Identify the preparation type.
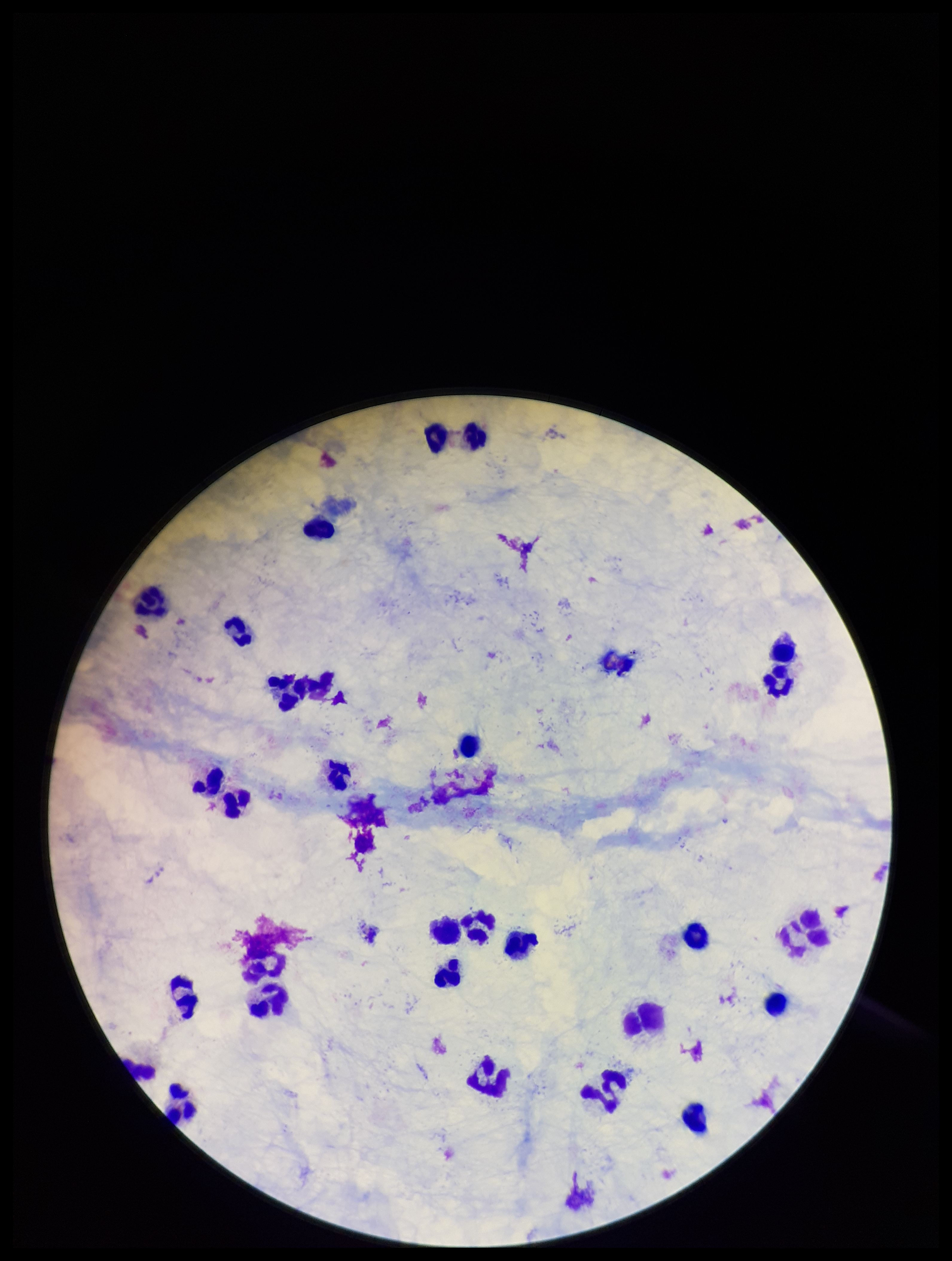

Thick.

Summary:
  - Patient malaria status: negative
  - Stain: Giemsa
  - Field of view: single
  - Capture: smartphone photograph through the microscope eyepiece
  - Parasite count: 0
  - Plasmodium parasites: none identified
  - Leukocyte count: 26
  - Image size: 952×1261 pixels